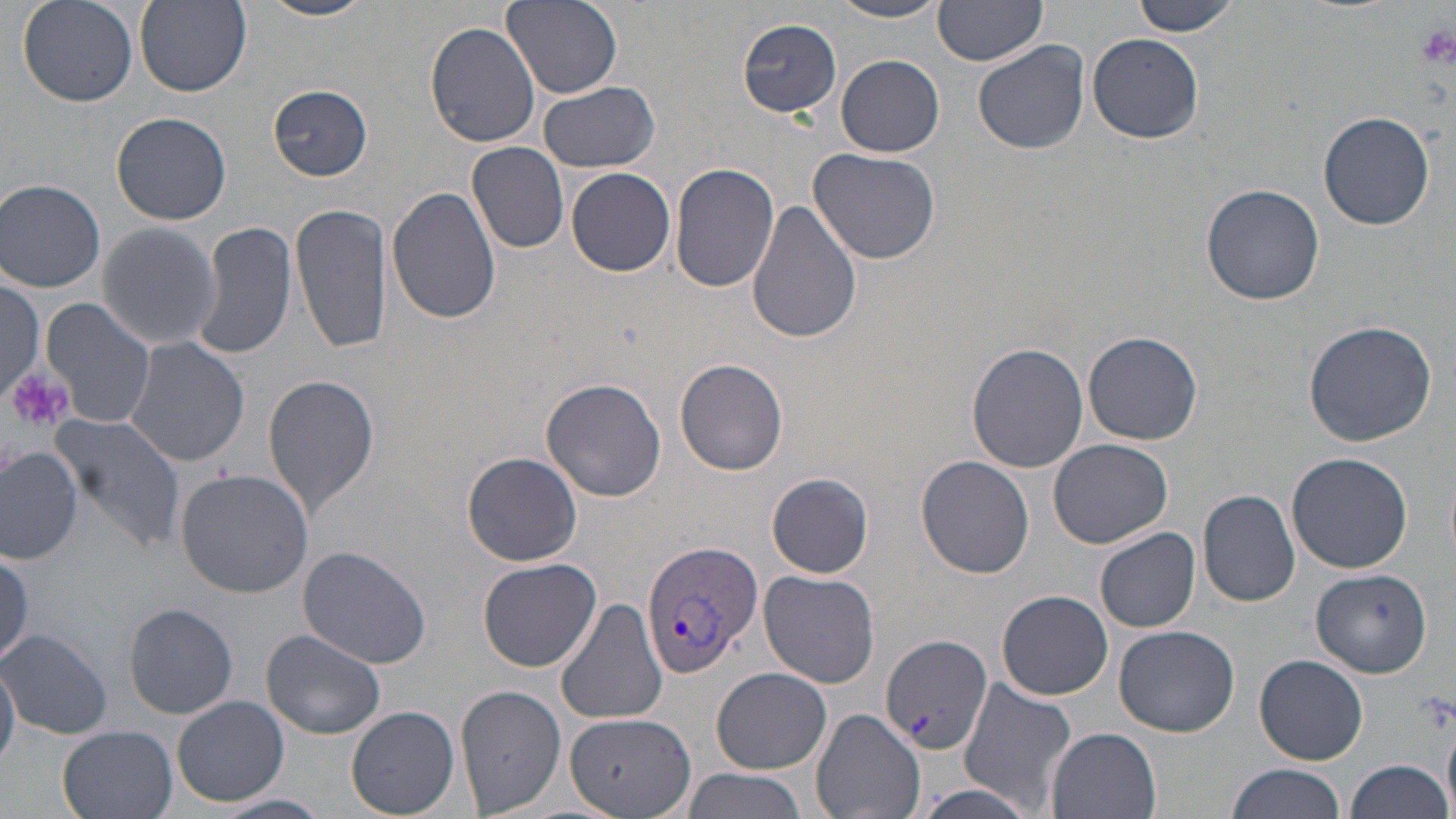
Approximate bounding boxes as named x1/y1/x2/y2 corners in pixels. Plasmodium vivax-infected red blood cell locations: (x1=641, y1=538, x2=762, y2=680). Uninfected red blood cell locations: (x1=16, y1=0, x2=140, y2=109), (x1=135, y1=0, x2=250, y2=96), (x1=257, y1=0, x2=377, y2=22), (x1=502, y1=0, x2=623, y2=98), (x1=932, y1=1, x2=1049, y2=69), (x1=1128, y1=1, x2=1241, y2=38), (x1=827, y1=2, x2=951, y2=23), (x1=736, y1=18, x2=841, y2=117), (x1=426, y1=22, x2=541, y2=149), (x1=1087, y1=32, x2=1204, y2=143), (x1=973, y1=39, x2=1089, y2=154), (x1=836, y1=55, x2=945, y2=157), (x1=536, y1=79, x2=660, y2=172), (x1=268, y1=85, x2=371, y2=180), (x1=112, y1=111, x2=232, y2=224), (x1=1319, y1=111, x2=1436, y2=229), (x1=467, y1=141, x2=570, y2=253), (x1=808, y1=147, x2=942, y2=265), (x1=409, y1=158, x2=541, y2=293), (x1=670, y1=162, x2=779, y2=292), (x1=565, y1=167, x2=676, y2=276), (x1=1, y1=178, x2=107, y2=292), (x1=1201, y1=181, x2=1327, y2=305), (x1=386, y1=186, x2=502, y2=324), (x1=747, y1=198, x2=863, y2=345), (x1=290, y1=202, x2=392, y2=353), (x1=96, y1=221, x2=221, y2=350), (x1=189, y1=222, x2=297, y2=361), (x1=0, y1=279, x2=45, y2=405), (x1=41, y1=298, x2=153, y2=429), (x1=1303, y1=319, x2=1437, y2=447), (x1=1083, y1=330, x2=1203, y2=444), (x1=124, y1=337, x2=251, y2=466), (x1=967, y1=340, x2=1090, y2=472), (x1=676, y1=357, x2=788, y2=476), (x1=263, y1=374, x2=380, y2=516), (x1=540, y1=378, x2=670, y2=503), (x1=47, y1=411, x2=188, y2=552), (x1=1049, y1=438, x2=1174, y2=548), (x1=0, y1=445, x2=83, y2=565), (x1=461, y1=452, x2=583, y2=567), (x1=1286, y1=452, x2=1415, y2=574), (x1=916, y1=455, x2=1034, y2=578), (x1=176, y1=468, x2=315, y2=598), (x1=768, y1=474, x2=871, y2=576), (x1=1197, y1=490, x2=1302, y2=607), (x1=1095, y1=527, x2=1201, y2=632), (x1=297, y1=546, x2=434, y2=668), (x1=0, y1=547, x2=32, y2=666), (x1=478, y1=557, x2=600, y2=672), (x1=1309, y1=568, x2=1432, y2=677), (x1=759, y1=570, x2=880, y2=687), (x1=998, y1=589, x2=1114, y2=699), (x1=554, y1=594, x2=670, y2=726), (x1=124, y1=603, x2=238, y2=717), (x1=1113, y1=624, x2=1240, y2=735), (x1=0, y1=629, x2=111, y2=739), (x1=262, y1=629, x2=387, y2=739), (x1=880, y1=633, x2=992, y2=755), (x1=1253, y1=654, x2=1368, y2=765), (x1=0, y1=657, x2=20, y2=769), (x1=712, y1=667, x2=835, y2=774), (x1=956, y1=679, x2=1077, y2=814), (x1=456, y1=682, x2=568, y2=815), (x1=173, y1=695, x2=289, y2=806), (x1=346, y1=706, x2=460, y2=818), (x1=812, y1=708, x2=926, y2=819), (x1=564, y1=716, x2=695, y2=816), (x1=1443, y1=722, x2=1455, y2=816), (x1=57, y1=725, x2=181, y2=819), (x1=1043, y1=726, x2=1164, y2=819), (x1=1345, y1=760, x2=1452, y2=819), (x1=1225, y1=762, x2=1348, y2=819), (x1=678, y1=768, x2=806, y2=819). Platelet locations: (x1=1416, y1=22, x2=1456, y2=70), (x1=8, y1=370, x2=74, y2=433). Slide-level diagnosis: Plasmodium vivax. Single field of view. Image is 1456×819 pixels. May-Grünwald-Giemsa stain. Captured at 1000x magnification. Optical microscopy. Thin blood smear.